Locate every white blood cell.
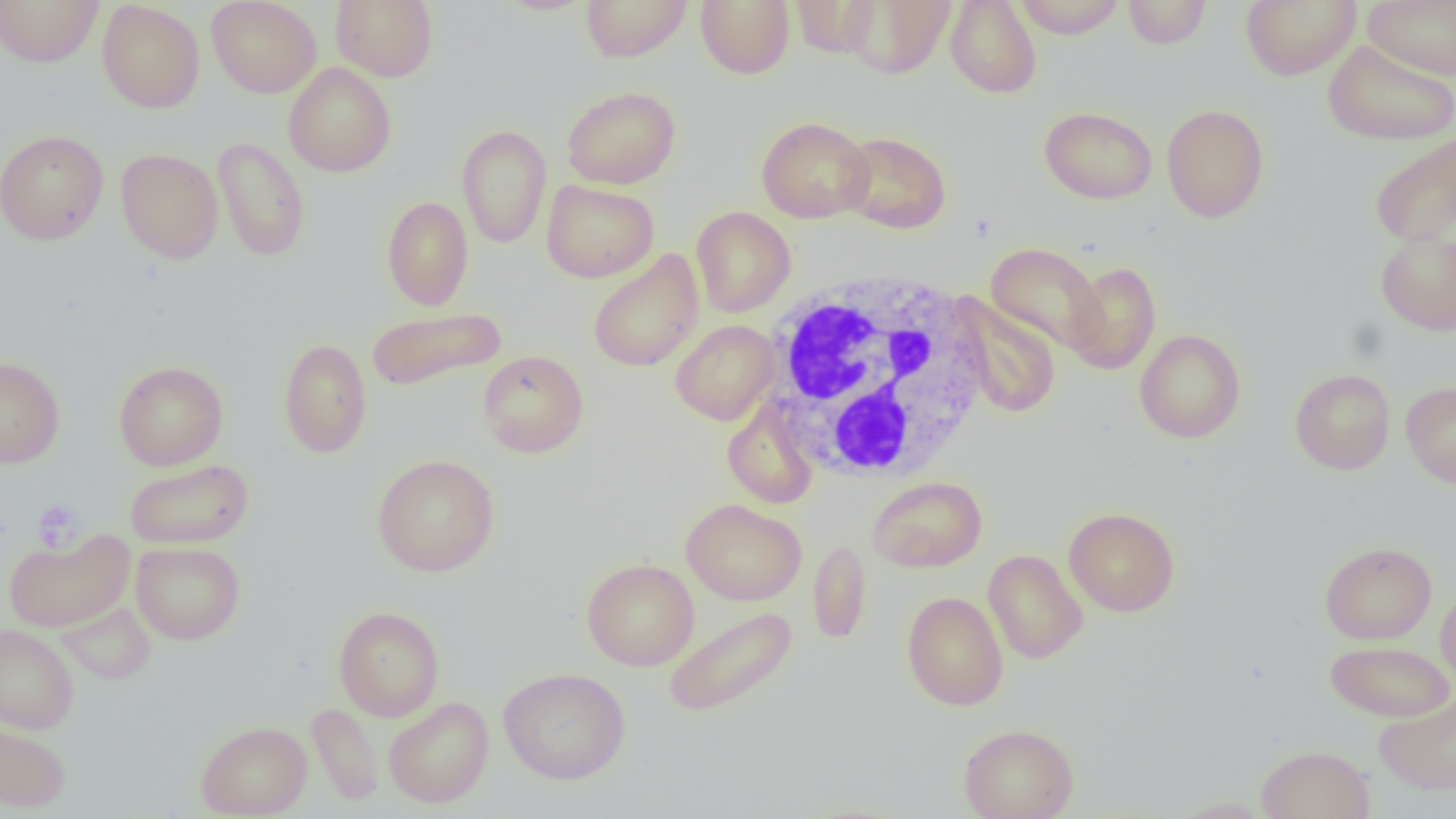

Approximate bounding boxes as named x1/y1/x2/y2 corners in pixels.
White blood cells: (x1=761, y1=272, x2=992, y2=484).

slide-level diagnosis = negative for blood parasites
modality = light microscopy
preparation = thin blood smear
magnification = 1000x
uninfected red blood cell locations = approximate bounding boxes as named x1/y1/x2/y2 corners in pixels: (x1=0, y1=0, x2=104, y2=67), (x1=207, y1=0, x2=322, y2=98), (x1=330, y1=0, x2=438, y2=82), (x1=581, y1=0, x2=692, y2=62), (x1=695, y1=0, x2=794, y2=79), (x1=842, y1=0, x2=955, y2=79), (x1=945, y1=0, x2=1041, y2=98), (x1=1014, y1=0, x2=1126, y2=38), (x1=1123, y1=0, x2=1211, y2=50), (x1=1241, y1=0, x2=1360, y2=80), (x1=1364, y1=0, x2=1455, y2=80), (x1=97, y1=1, x2=205, y2=113), (x1=492, y1=1, x2=597, y2=16), (x1=790, y1=1, x2=879, y2=57), (x1=1323, y1=39, x2=1456, y2=146), (x1=283, y1=62, x2=396, y2=177), (x1=562, y1=86, x2=681, y2=189), (x1=1161, y1=104, x2=1269, y2=223), (x1=1039, y1=106, x2=1157, y2=204), (x1=757, y1=116, x2=875, y2=223), (x1=456, y1=125, x2=552, y2=249), (x1=0, y1=129, x2=109, y2=245), (x1=838, y1=131, x2=951, y2=234), (x1=1369, y1=133, x2=1456, y2=247), (x1=213, y1=137, x2=309, y2=261), (x1=116, y1=148, x2=224, y2=263), (x1=541, y1=179, x2=659, y2=283), (x1=382, y1=196, x2=473, y2=311), (x1=691, y1=206, x2=795, y2=317), (x1=1376, y1=229, x2=1456, y2=336), (x1=986, y1=242, x2=1105, y2=355), (x1=587, y1=249, x2=704, y2=373), (x1=1065, y1=261, x2=1161, y2=374), (x1=951, y1=295, x2=1061, y2=418), (x1=365, y1=307, x2=507, y2=391), (x1=670, y1=320, x2=780, y2=425), (x1=1135, y1=329, x2=1246, y2=443), (x1=278, y1=338, x2=371, y2=458), (x1=477, y1=350, x2=589, y2=458), (x1=0, y1=356, x2=65, y2=468), (x1=114, y1=361, x2=228, y2=470), (x1=1289, y1=368, x2=1395, y2=475), (x1=1400, y1=381, x2=1456, y2=488), (x1=722, y1=399, x2=820, y2=509), (x1=372, y1=454, x2=500, y2=577), (x1=125, y1=458, x2=254, y2=549), (x1=867, y1=476, x2=987, y2=572), (x1=681, y1=498, x2=806, y2=605), (x1=1064, y1=507, x2=1180, y2=616), (x1=4, y1=529, x2=134, y2=632), (x1=808, y1=539, x2=871, y2=644), (x1=131, y1=541, x2=245, y2=645), (x1=1319, y1=541, x2=1436, y2=644), (x1=983, y1=549, x2=1088, y2=664), (x1=581, y1=558, x2=699, y2=671), (x1=1435, y1=586, x2=1456, y2=688), (x1=901, y1=591, x2=1008, y2=710), (x1=57, y1=601, x2=156, y2=685), (x1=333, y1=606, x2=444, y2=721), (x1=663, y1=606, x2=797, y2=719), (x1=0, y1=624, x2=79, y2=734), (x1=1325, y1=639, x2=1455, y2=722), (x1=498, y1=667, x2=631, y2=785), (x1=1374, y1=693, x2=1456, y2=795), (x1=383, y1=696, x2=494, y2=808), (x1=307, y1=702, x2=384, y2=806), (x1=0, y1=716, x2=72, y2=812), (x1=195, y1=720, x2=312, y2=818), (x1=958, y1=723, x2=1078, y2=819), (x1=1256, y1=745, x2=1375, y2=819), (x1=1167, y1=797, x2=1275, y2=818)
platelet locations = approximate bounding boxes as named x1/y1/x2/y2 corners in pixels: (x1=31, y1=498, x2=84, y2=552)
image size = 1456×819 pixels
field of view = one of a larger specimen